Report the malaria status of this cell.
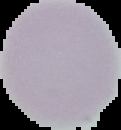
It is uninfected.

The area outside the segmented cell region is set to black. Image is 121×130 pixels. From a thin blood film.